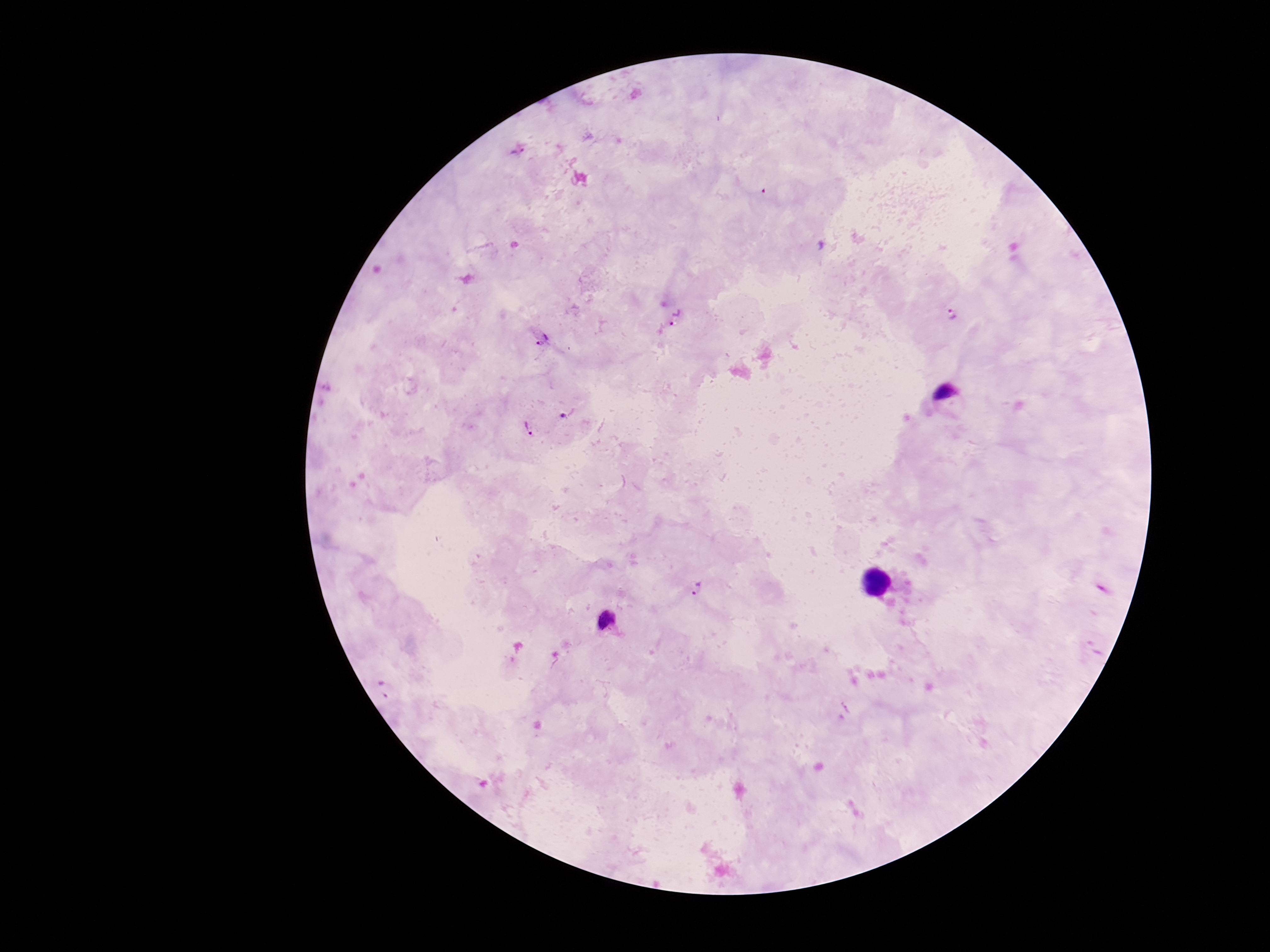

Plasmodium parasite locations = approximate centers as (x, y) in pixels: (518, 152), (952, 315), (678, 318), (544, 341), (568, 413), (528, 428), (697, 589), (606, 619)
field of view = single
image size = 1270×952 pixels
patient malaria status = positive
magnification = 100x
capture = smartphone camera through the microscope eyepiece
preparation = thick peripheral-blood smear
stain = Giemsa